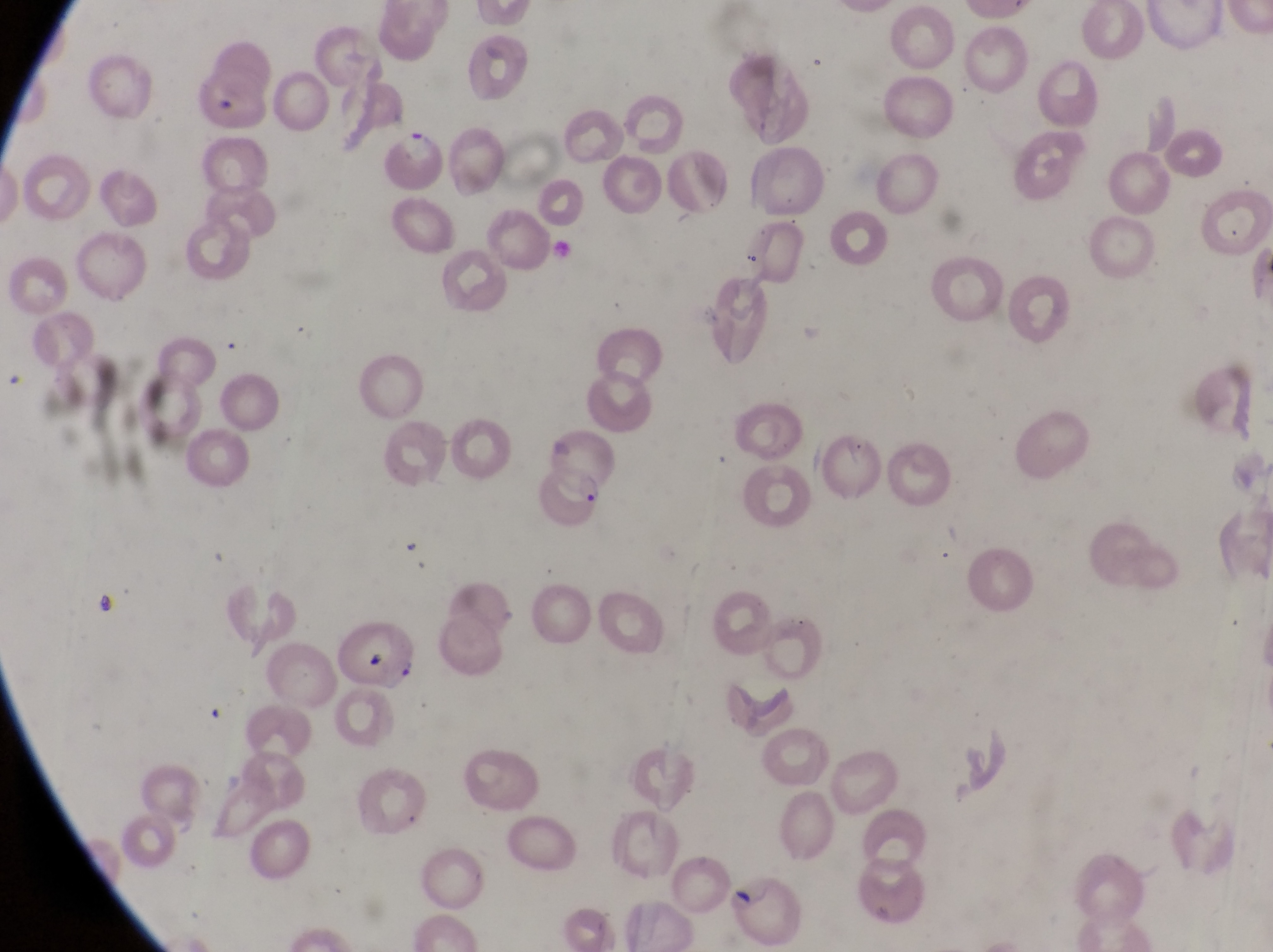 Approximate bounding boxes as {left, top, right, bottom} in pixels. Artifact (platelet-like body, stain precipitate, or debris) locations: {364, 652, 396, 680}. Parasitised red blood cell locations: {387, 130, 444, 186}, {537, 460, 606, 527}, {731, 876, 801, 946}. Captured by a smartphone held over the eyepiece of an Olympus CX-23 microscope. Thin blood film. Collected in Uganda. Magnification of 1000x. Image is 1273×952 pixels. One field of view.